Identify the preparation type.
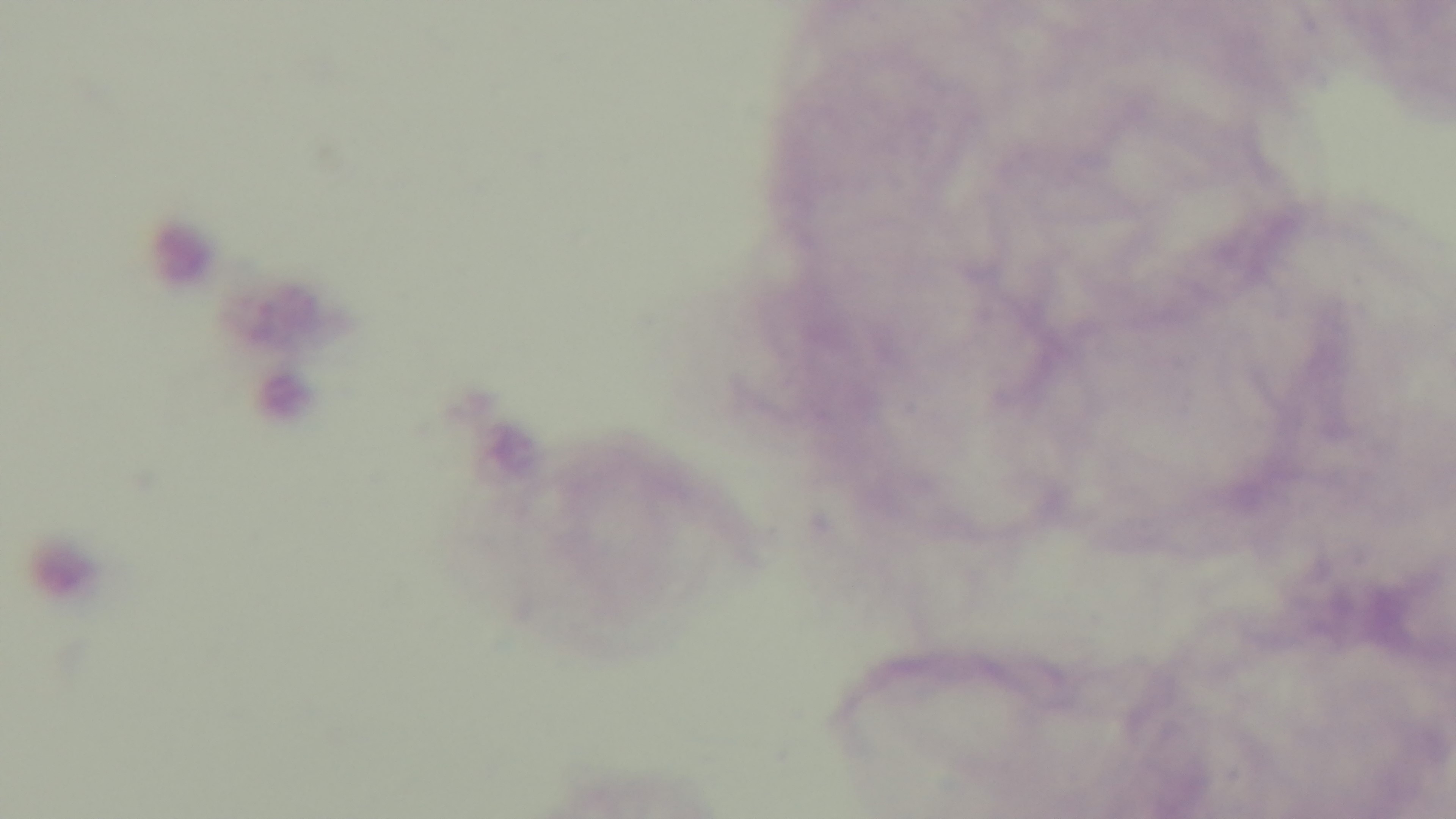

A thick smear.

capture = mounted 4K digital camera
objective = 100x oil immersion
stain = Giemsa
malaria status = negative
field of view = single
modality = light microscopy